Assess this cell for malaria.
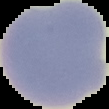

Uninfected.

preparation = thin blood film
image type = segmented cell region with the area outside set to black
image size = 109×109 pixels